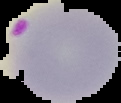
Image is 121×103 pixels. Segmented cell region on a black background. Malaria status: parasitized. From a thin blood smear.